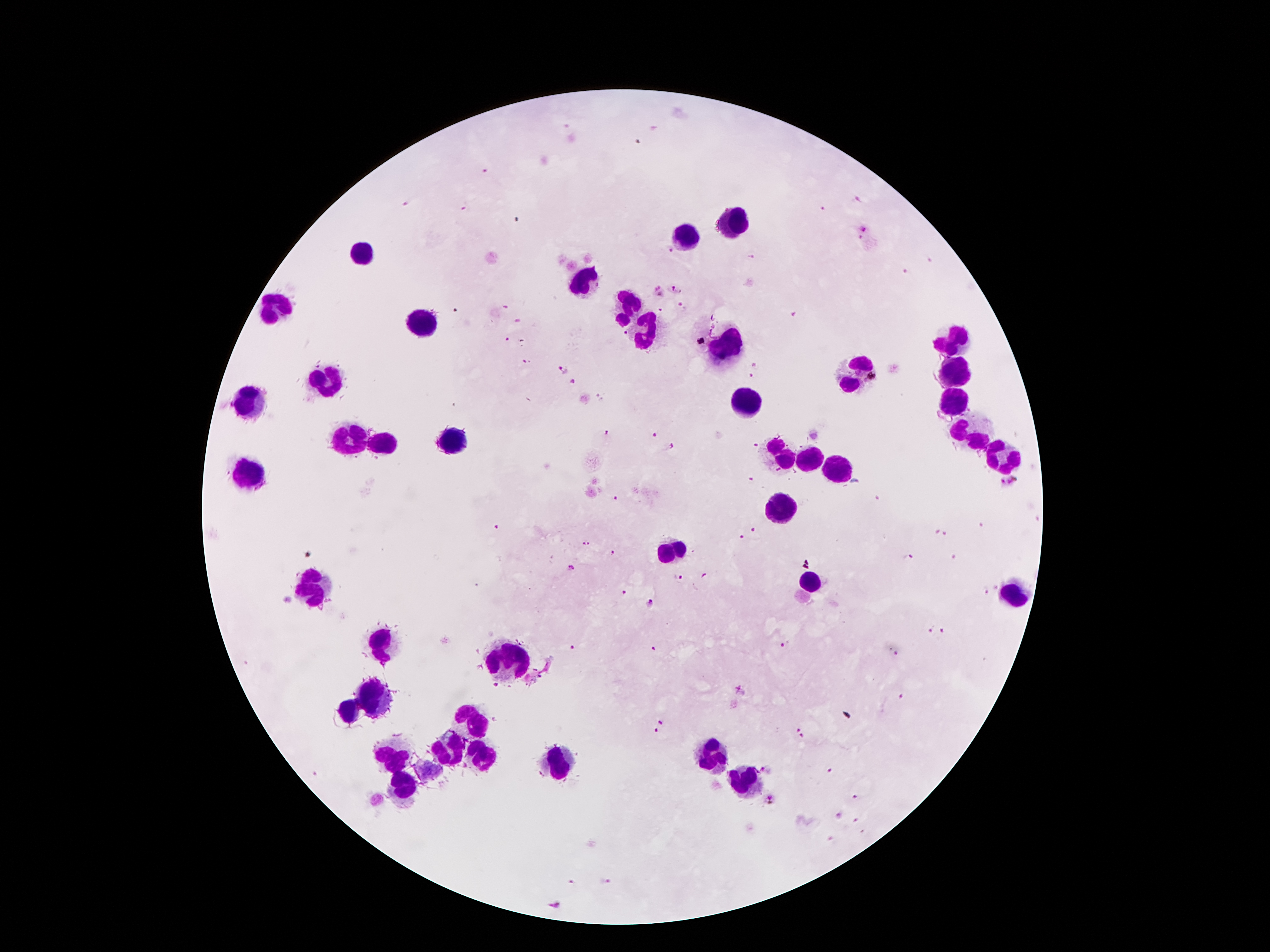
coordinate format = approximate centers as [x, y] in pixels
leukocyte locations = [736, 223], [687, 234], [359, 255], [580, 279], [272, 306], [627, 311], [424, 323], [645, 334], [955, 342], [725, 349], [853, 374], [951, 376], [326, 384], [249, 400], [743, 402], [953, 404], [969, 432], [351, 440], [452, 442], [382, 447], [998, 454], [780, 456], [808, 461], [837, 467], [253, 474], [778, 509], [675, 551], [811, 580], [312, 593], [1012, 594], [382, 643], [512, 657], [375, 694], [349, 710], [473, 720], [449, 748], [391, 757], [713, 757], [484, 761], [557, 762], [746, 780], [401, 789]
malaria parasite locations = [639, 142], [486, 171], [858, 199], [405, 203], [463, 209], [821, 211], [862, 229], [860, 238], [671, 252], [753, 257], [930, 261], [904, 273], [676, 290], [658, 293], [682, 304], [508, 308], [660, 310], [791, 315], [519, 321], [624, 333], [509, 339], [527, 361], [754, 365], [563, 368], [753, 377], [571, 381], [605, 435], [652, 436], [754, 445], [670, 449], [750, 481], [1007, 482], [616, 497], [880, 499], [983, 526], [495, 528], [755, 530], [937, 531], [743, 536], [947, 536], [586, 543], [612, 553], [307, 554], [953, 557], [909, 558], [573, 566], [704, 577], [677, 579], [994, 588], [982, 590], [623, 593], [650, 605], [929, 629], [943, 632], [785, 645], [575, 649], [654, 649], [897, 653], [497, 686], [740, 690], [495, 718], [661, 720], [798, 728], [657, 730], [801, 736], [765, 770], [829, 771], [854, 797], [770, 799], [839, 816], [856, 821], [830, 839], [571, 883], [606, 884], [553, 906]
stain = Giemsa
image size = 1270×952 pixels
preparation = thick peripheral-blood smear
field of view = single
capture = smartphone through the microscope eyepiece
patient malaria status = positive for Plasmodium falciparum
magnification = 100x